Locate and identify every blood parasite.
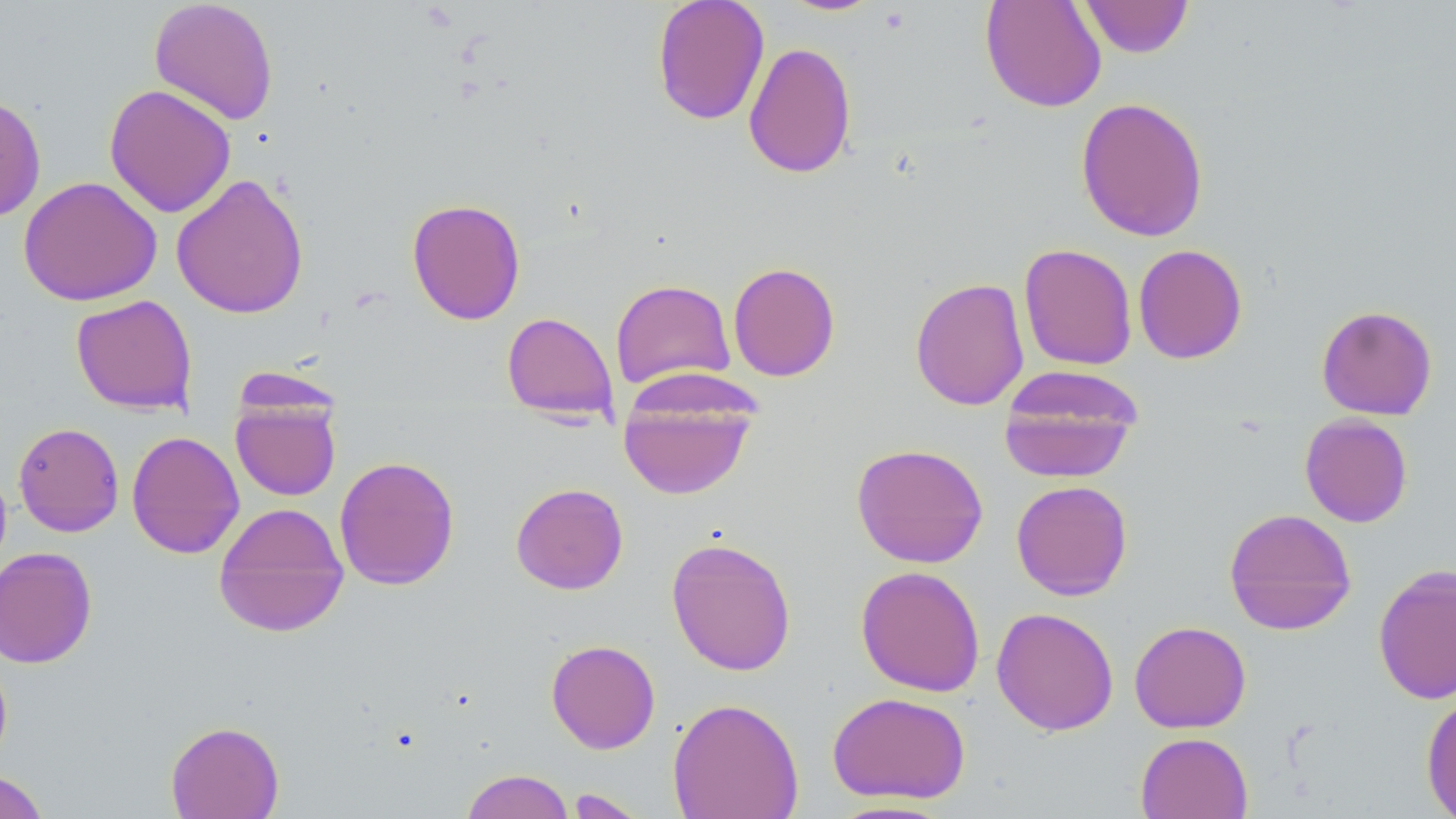
No blood parasites seen.

Approximate bounding boxes as (x1, y1, x2, y2) in pixels. Uninfected red blood cell locations: (149, 0, 279, 125), (651, 0, 770, 126), (778, 0, 885, 17), (980, 0, 1107, 113), (1079, 0, 1194, 58), (743, 41, 857, 179), (104, 84, 236, 218), (0, 93, 47, 223), (1075, 96, 1209, 242), (171, 173, 309, 319), (18, 175, 162, 306), (406, 198, 526, 325), (1019, 243, 1137, 371), (1133, 243, 1248, 364), (727, 261, 840, 382), (910, 277, 1029, 411), (610, 279, 736, 390), (70, 294, 198, 415), (1316, 304, 1438, 420), (501, 311, 619, 420), (998, 365, 1144, 483), (616, 373, 761, 501), (230, 396, 341, 501), (1299, 413, 1413, 527), (13, 422, 124, 537), (126, 430, 245, 559), (851, 442, 989, 569), (333, 455, 460, 590), (1011, 480, 1133, 600), (510, 482, 629, 595), (213, 502, 350, 637), (1223, 508, 1358, 635), (666, 536, 797, 676), (0, 546, 98, 669), (1372, 564, 1456, 705), (855, 565, 985, 697), (991, 606, 1119, 736), (1129, 620, 1251, 734), (546, 639, 660, 754), (827, 691, 971, 805), (1420, 691, 1456, 819), (667, 696, 804, 819), (165, 720, 285, 818), (1135, 732, 1253, 819), (1, 769, 50, 819), (460, 769, 575, 819), (564, 788, 649, 818). Slide-level diagnosis: negative for blood parasites. May-Grünwald-Giemsa stain. Light microscopy. Single field of view. Thin blood film. Captured at 1000x magnification. Image is 1456×819 pixels.